Give the position of every Plasmodium parasite visible.
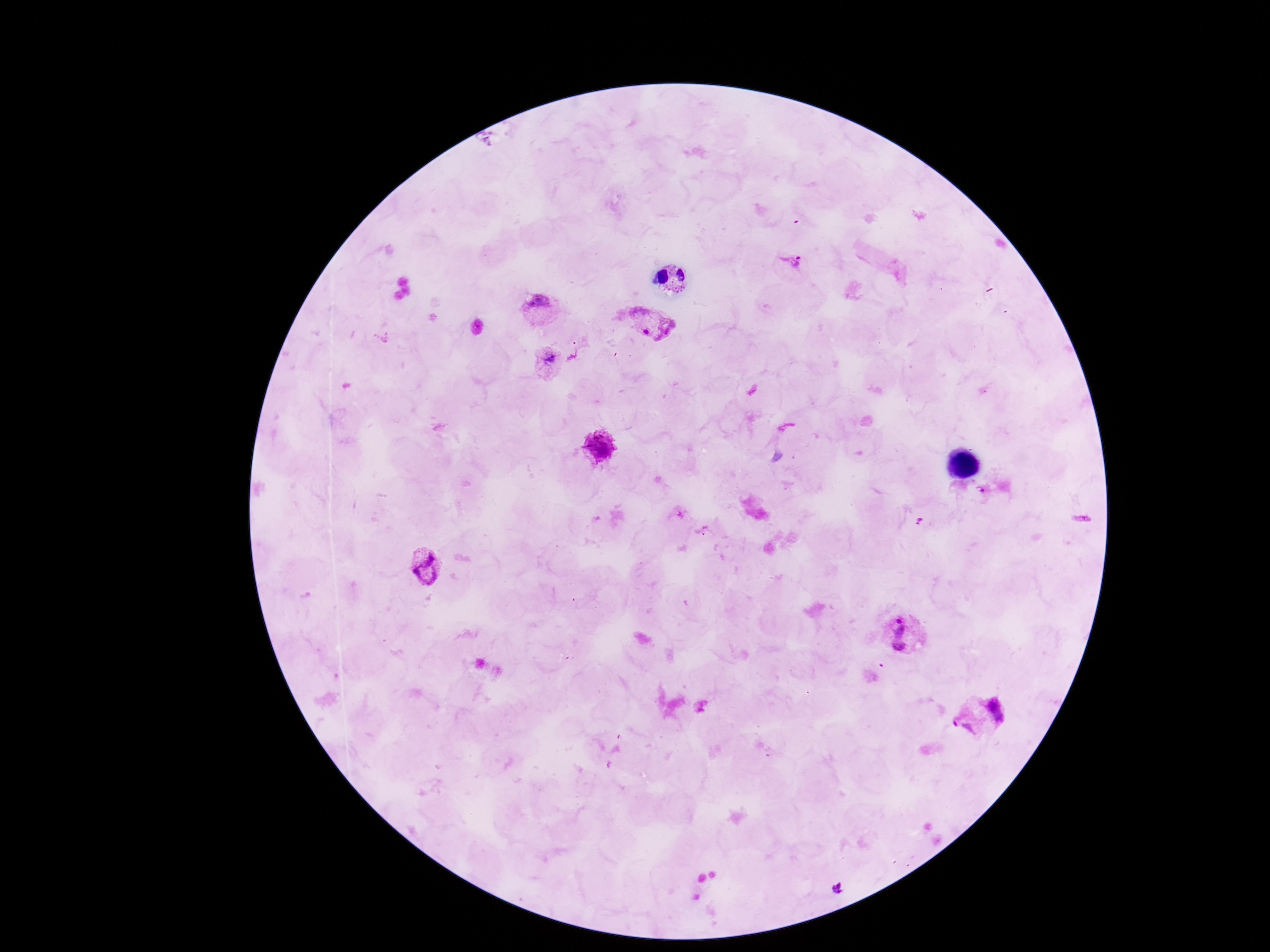

Approximate centers as {x, y} in pixels.
Plasmodium parasites: {791, 264}, {542, 309}, {651, 324}, {547, 361}, {599, 448}, {982, 491}, {429, 566}, {905, 634}, {981, 718}, {839, 890}.

Summary:
  - Patient malaria status: positive
  - Preparation: thick peripheral-blood smear
  - Field of view: one from this slide
  - Capture: smartphone camera through the microscope eyepiece
  - Image size: 1270×952 pixels
  - Stain: Giemsa
  - Magnification: 100x